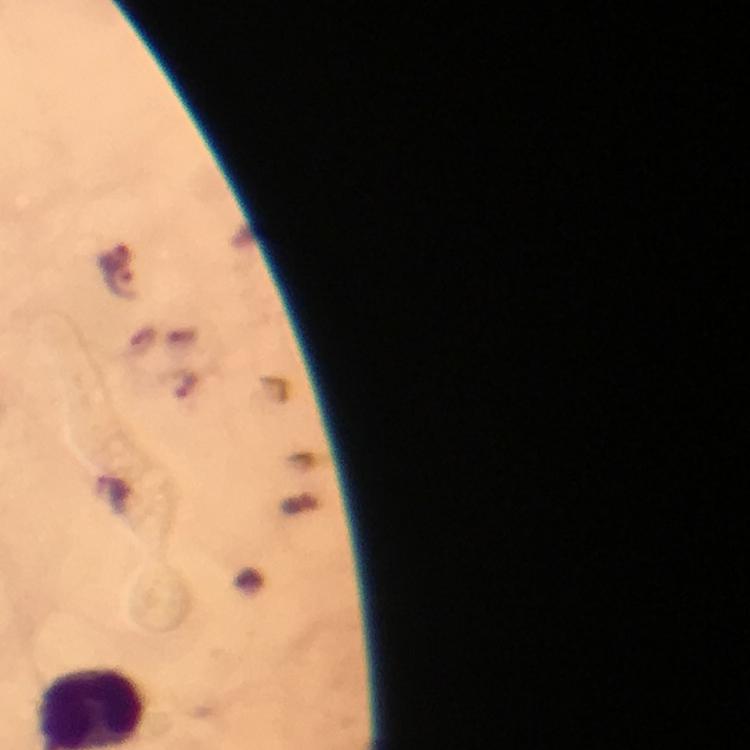 Approximate centers as (x, y) in pixels. Malaria parasite locations: (121, 282). Photographed with a smartphone mounted on the microscope. Thick blood film. From a diagnostic examination for malaria. Immersion oil was used. A crop from one field of view. At 100x magnification. Image is 750×750 pixels. Giemsa stain.